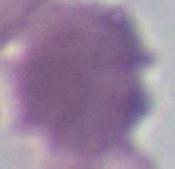 Captured at 1000x magnification. An erythrocyte is seen. Micrograph.